Locate every blood parasite and identify its species.
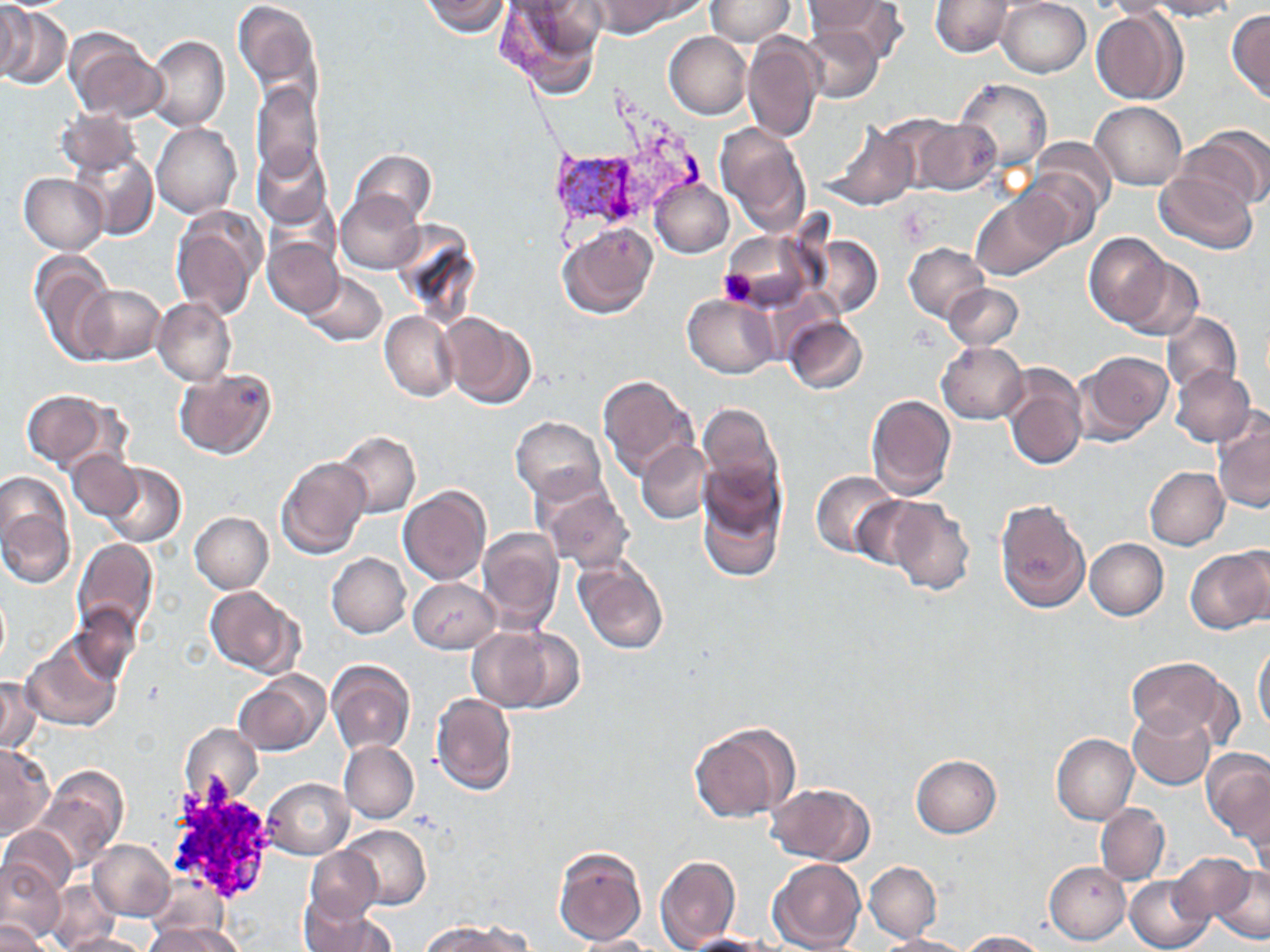

Approximate bounding boxes as (x1, y1, x2, y2) in pixels.
Plasmodium vivax-infected red blood cells: (551, 150, 655, 226).
No Plasmodium falciparum, Plasmodium ovale, Plasmodium malariae, Babesia divergens, or Trypanosoma brucei observed.

Uninfected red blood cell locations: (0, 0, 31, 82), (234, 0, 325, 110), (420, 0, 512, 37), (496, 0, 605, 98), (591, 0, 699, 35), (706, 0, 796, 45), (803, 0, 903, 56), (997, 0, 1090, 77), (1144, 0, 1240, 20), (929, 1, 1017, 57), (0, 2, 71, 92), (1227, 8, 1269, 102), (1092, 10, 1183, 106), (798, 22, 883, 103), (65, 29, 166, 122), (663, 31, 751, 119), (145, 35, 230, 132), (742, 35, 823, 144), (954, 78, 1053, 176), (251, 82, 324, 184), (1091, 102, 1188, 190), (58, 107, 141, 176), (911, 115, 1001, 197), (822, 120, 918, 211), (152, 121, 242, 218), (715, 121, 814, 237), (1174, 125, 1269, 219), (1030, 136, 1115, 219), (252, 143, 335, 231), (78, 150, 158, 242), (350, 150, 436, 229), (1154, 167, 1259, 254), (1016, 171, 1100, 250), (18, 173, 108, 254), (651, 178, 733, 257), (336, 191, 424, 275), (971, 194, 1064, 280), (171, 206, 267, 321), (556, 225, 658, 319), (721, 228, 820, 315), (1086, 233, 1175, 329), (809, 235, 882, 316), (264, 238, 344, 317), (904, 243, 990, 322), (29, 248, 119, 363), (1116, 255, 1204, 340), (299, 271, 387, 347), (942, 280, 1023, 349), (75, 282, 165, 365), (684, 294, 778, 377), (154, 298, 235, 386), (379, 311, 459, 400), (437, 312, 535, 410), (1163, 312, 1243, 398), (784, 317, 870, 394), (937, 342, 1027, 424), (1076, 349, 1173, 444), (1001, 364, 1088, 471), (1169, 367, 1257, 448), (173, 368, 277, 461), (598, 375, 698, 479), (23, 389, 115, 470), (867, 392, 957, 500), (695, 398, 786, 572), (1213, 409, 1270, 516), (511, 415, 606, 501), (337, 432, 421, 518), (637, 439, 712, 525), (68, 448, 141, 521), (276, 454, 371, 559), (102, 462, 185, 548), (1145, 466, 1228, 549), (810, 470, 905, 560), (535, 476, 636, 572), (0, 481, 75, 586), (397, 484, 493, 585), (849, 496, 935, 574), (882, 497, 975, 596), (996, 497, 1091, 614), (188, 511, 272, 592), (194, 511, 282, 670), (478, 527, 565, 635), (73, 537, 160, 646), (1084, 537, 1168, 620), (1186, 546, 1270, 634), (327, 554, 410, 637), (574, 556, 670, 655), (408, 577, 500, 654), (204, 585, 300, 674), (1, 590, 10, 668), (71, 603, 145, 688), (467, 626, 577, 713), (1253, 636, 1270, 739), (23, 639, 120, 731), (1126, 656, 1238, 747), (328, 660, 416, 755), (234, 669, 328, 756), (0, 676, 40, 755), (431, 692, 517, 795), (1127, 708, 1215, 789), (688, 720, 800, 823), (180, 723, 262, 808), (1051, 734, 1138, 824), (339, 741, 419, 823), (0, 742, 54, 838), (1201, 749, 1270, 846), (911, 754, 1002, 837), (33, 766, 128, 874), (263, 778, 354, 859), (762, 782, 873, 865), (1095, 804, 1169, 884), (337, 824, 431, 910), (1, 825, 77, 902), (89, 840, 175, 922), (553, 845, 648, 946), (305, 846, 382, 922), (1169, 850, 1257, 927), (655, 854, 741, 949), (771, 857, 866, 950), (0, 858, 64, 943), (1044, 859, 1131, 943), (864, 860, 941, 942), (1212, 865, 1270, 944), (1125, 875, 1213, 951), (48, 881, 119, 950), (298, 896, 396, 952), (0, 918, 49, 952), (423, 922, 516, 952), (141, 926, 231, 952), (958, 931, 1049, 951), (60, 933, 151, 952), (876, 933, 974, 952), (569, 934, 659, 952), (680, 935, 775, 951). Platelet locations: (719, 270, 758, 307). Slide-level diagnosis: Plasmodium vivax. One field of a larger specimen. Thin blood film. Captured at 1000x magnification. May-Grünwald-Giemsa stain. Optical microscopy. Image is 1270×952 pixels.